Assess this cell for malaria.
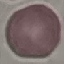
It is uninfected.

preparation: thin smear
capture: smartphone camera at the microscope eyepiece
image_type: cell patch, automatically extracted from a larger field of view and resized to 64 × 64 pixels
stain: Giemsa